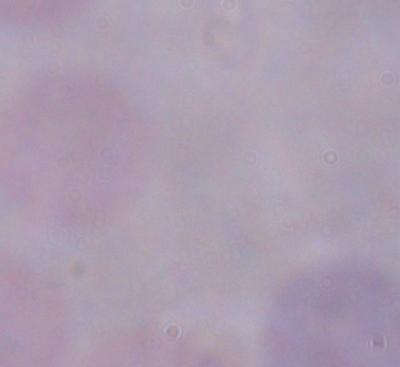
Summary:
  - Modality: photomicrograph
  - Magnification: 1000x
  - Identification: trypanosome